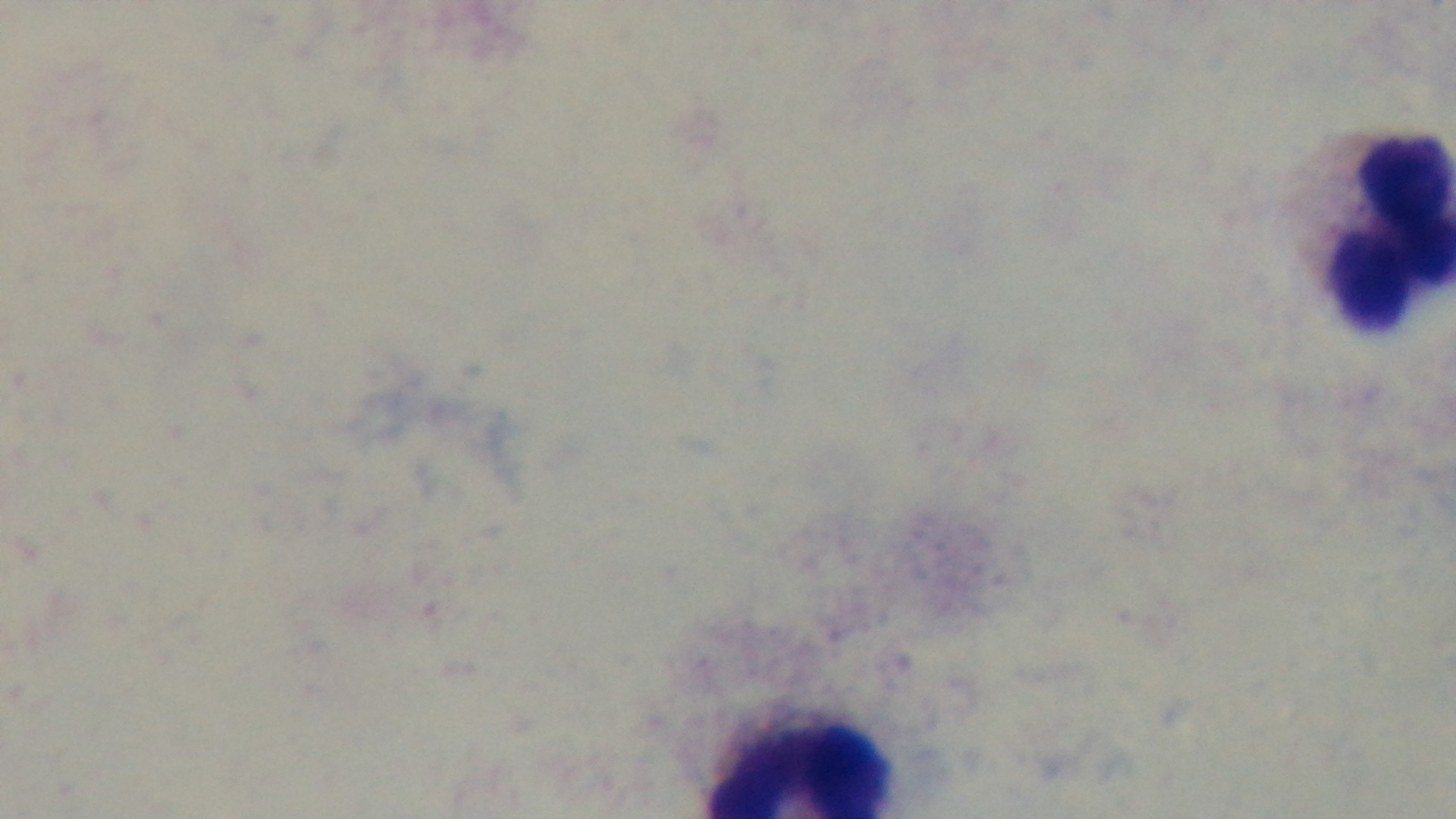
Summary:
  - Preparation: thick smear
  - Stain: Giemsa
  - Modality: light microscopy
  - Field of view: single
  - Malaria status: uninfected
  - Capture: mounted 4K digital camera
  - Objective: 100x oil immersion